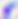
modality = micrograph
identification = Toxoplasma gondii
magnification = 400x